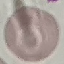

{
  "result": "negative for malaria parasites",
  "preparation": "thin blood smear",
  "stain": "Giemsa",
  "image_type": "cell patch, automatically extracted from a larger field of view and resized to 64 × 64 pixels",
  "capture": "smartphone through the microscope eyepiece"
}